Classify this cell by malaria status.
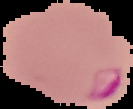
It is parasitized.

Summary:
  - Image size: 133×109 pixels
  - Image type: segmented cell region on a black background
  - Preparation: thin blood smear